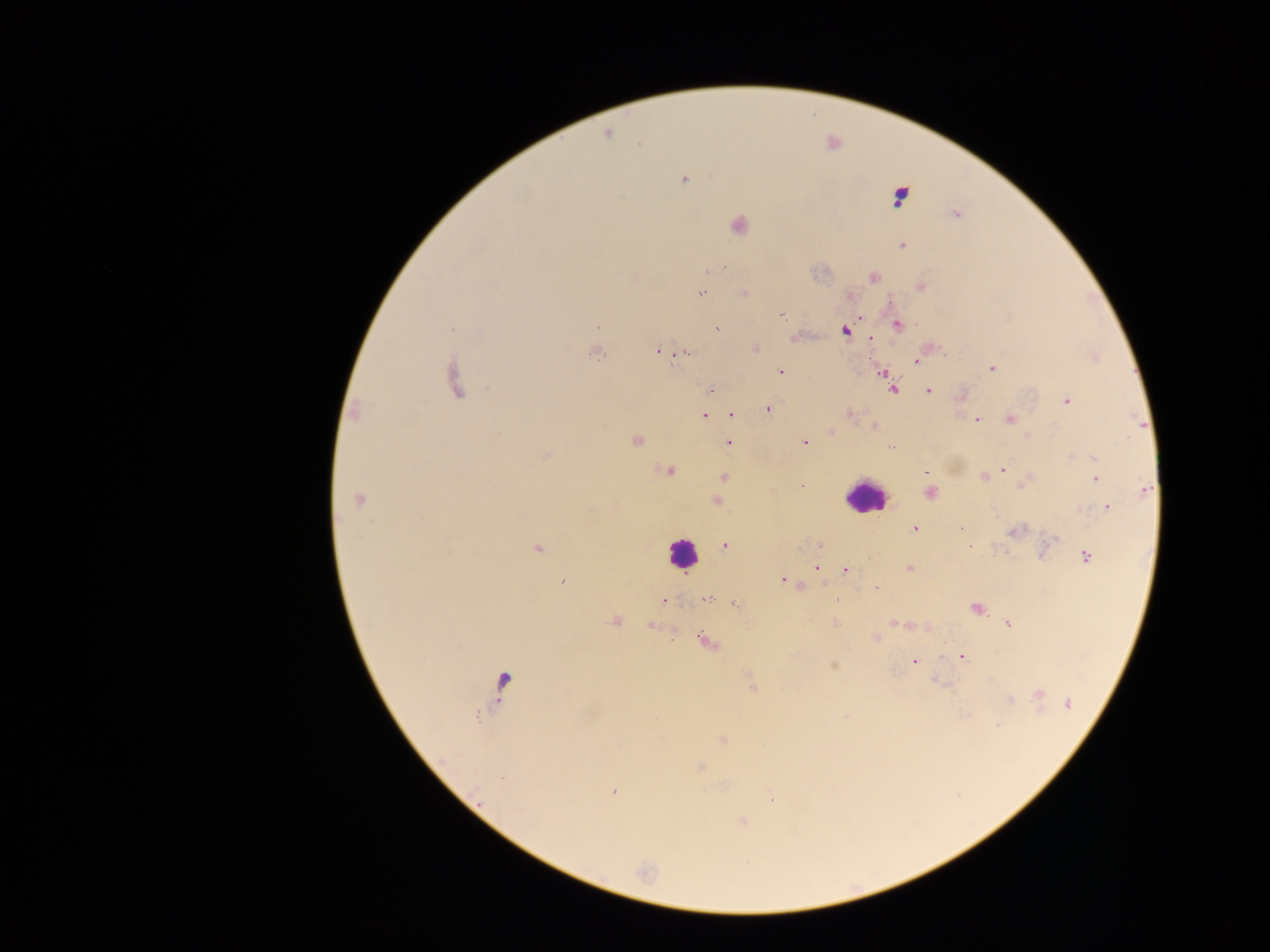

Approximate centers as (x, y) in pixels.
Summary:
  - Leukocyte locations: (864, 496), (682, 553)
  - Malaria parasite locations: (607, 133), (684, 179), (899, 197), (955, 214), (738, 225), (902, 246), (720, 268), (710, 270), (874, 277), (921, 287), (743, 293), (701, 294), (782, 316), (861, 318), (898, 325), (597, 326), (452, 329), (717, 329), (845, 331), (870, 338), (755, 349), (657, 351), (595, 353), (685, 353), (916, 362), (991, 368), (780, 372), (882, 372), (454, 381), (892, 389), (710, 390), (929, 391), (1067, 401), (768, 409), (355, 414), (849, 414), (704, 415), (731, 415), (976, 419), (1009, 420), (874, 427), (831, 431), (1028, 436), (636, 441), (728, 443), (805, 443), (890, 447), (546, 455), (1094, 458), (1002, 469), (669, 471), (927, 473), (724, 477), (984, 477), (1095, 479), (1026, 482), (1145, 490), (931, 493), (359, 499), (717, 500), (1107, 507), (914, 529), (1015, 531), (725, 545), (820, 546), (970, 546), (537, 548), (1086, 556), (817, 568), (909, 569), (845, 571), (783, 580), (563, 581), (877, 589), (708, 599), (663, 600), (838, 600), (734, 604), (976, 609), (615, 621), (835, 622), (1008, 623), (897, 624), (904, 625), (876, 637), (705, 641), (962, 657), (914, 661), (833, 666), (504, 683), (751, 685), (1039, 694), (1009, 699), (1068, 704), (998, 726), (723, 739), (700, 768), (502, 778), (614, 791), (772, 800), (741, 820)
  - Capture: mobile-phone photograph through a microscope
  - Country: Ghana
  - Image size: 1270×952 pixels
  - Field of view: single
  - Preparation: thick blood smear